Assess this cell for malaria.
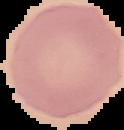
Uninfected.

From a thin blood film. The area outside the segmented cell region is set to black. Image is 124×130 pixels.